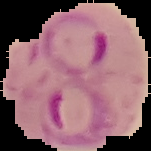

{
  "preparation": "thin blood film",
  "malaria_status": "parasitized",
  "image_type": "segmented cell region on a black background",
  "image_size": "151×151 pixels"
}